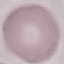
malaria status = uninfected
stain = Giemsa
capture = smartphone through the microscope eyepiece
preparation = thin blood film
image type = cell patch, automatically extracted from a larger field of view and resized to 64 × 64 pixels